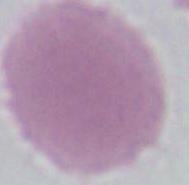

identification = erythrocyte
magnification = 1000x
modality = micrograph